Assess the morphology of the red blood cells.
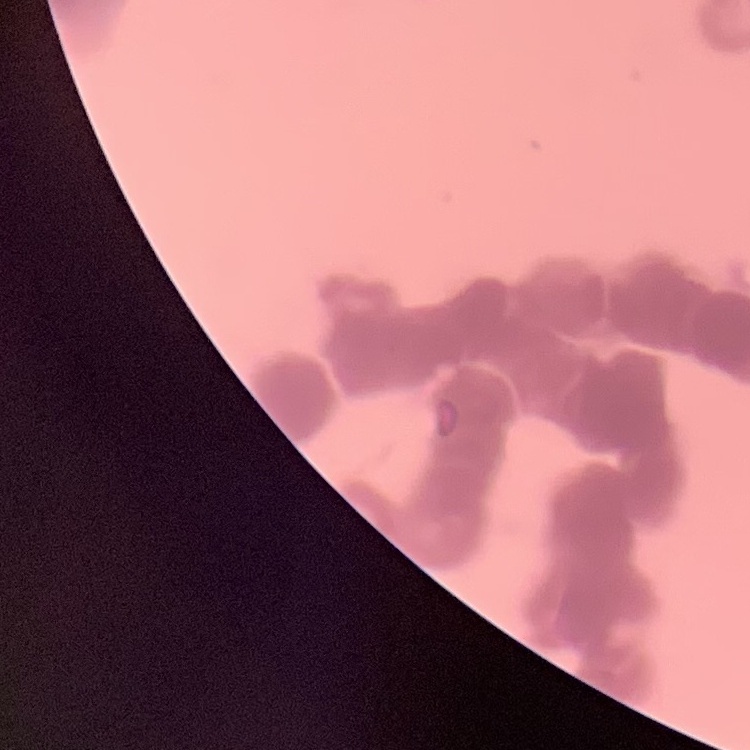
Rouleaux formation.

preparation = thin blood smear
stain = Field's or Giemsa
image type = square crop of a larger photomicrograph